Comment on the morphology of the erythrocytes.
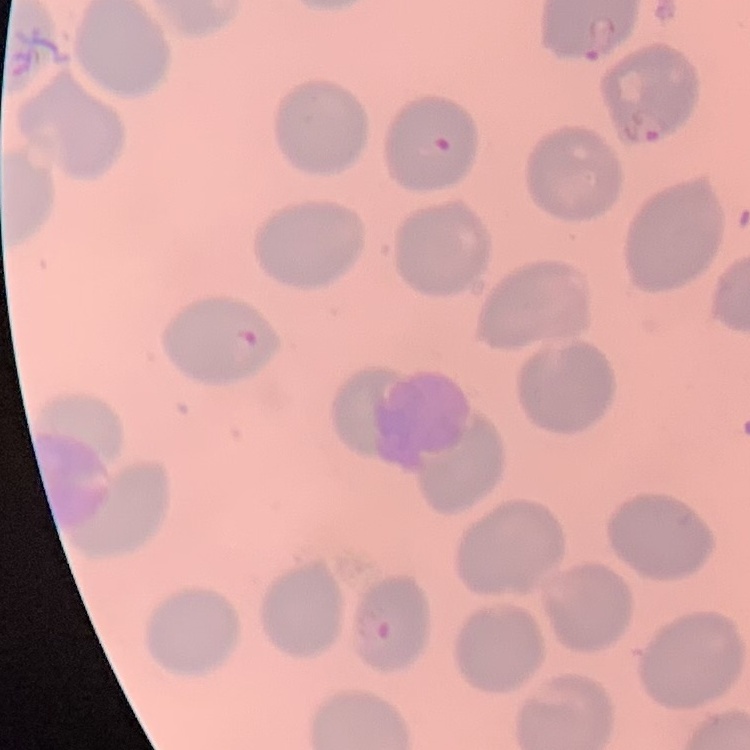

They show no rouleaux formation.

Summary:
  - Preparation: thin blood smear
  - Image type: one tile cut from a larger photomicrograph
  - Stain: Field's or Giemsa